Assess for malaria.
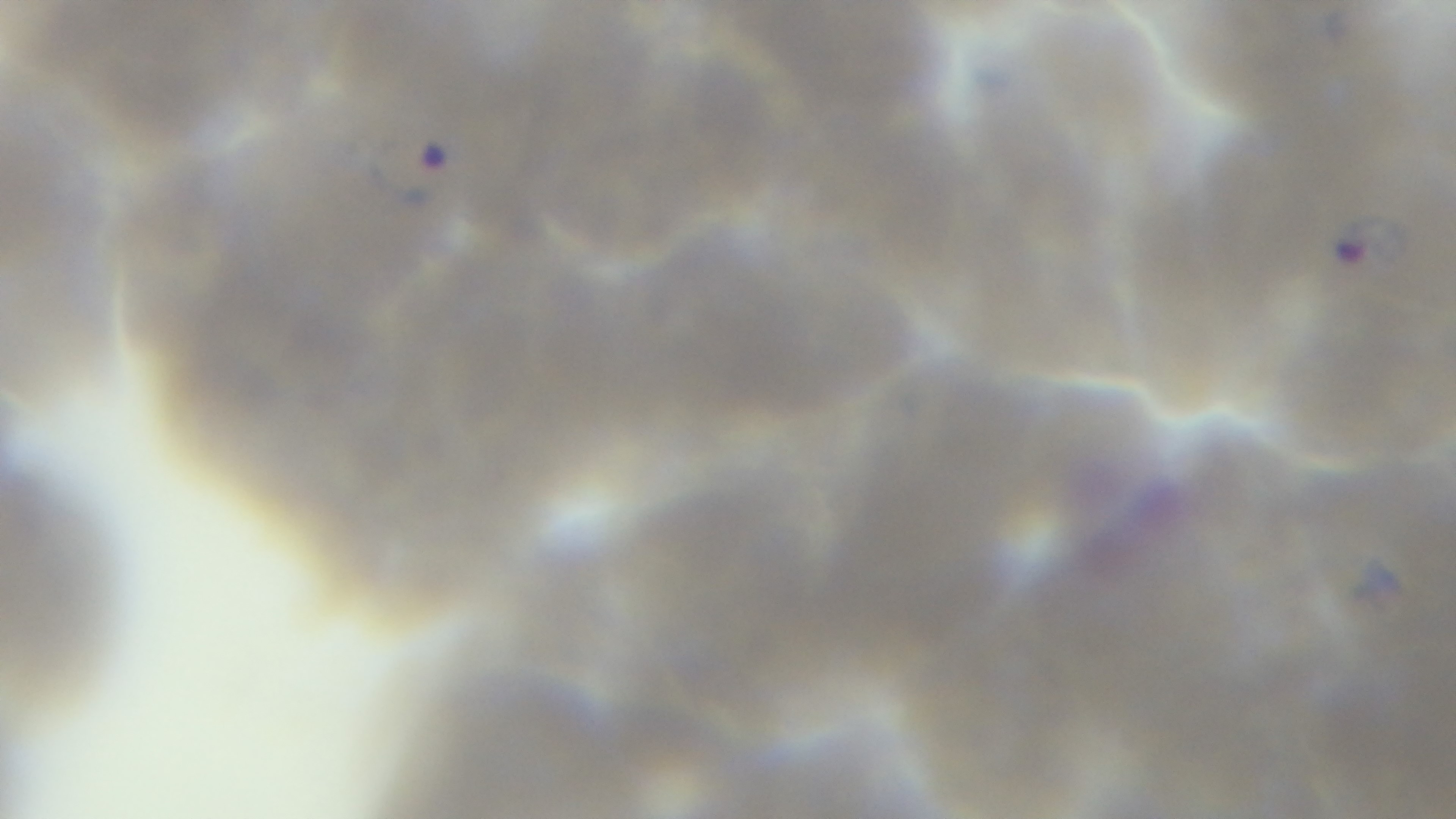

It is infected.

Summary:
  - Capture: mounted 4K digital camera
  - Preparation: thin blood film
  - Objective: 100x oil immersion
  - Modality: light microscopy
  - Field of view: single
  - Stain: Giemsa